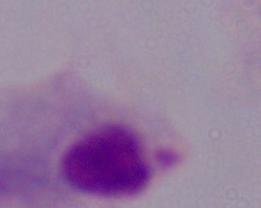
A trichomonad is seen. Micrograph. Captured at 1000x magnification.